Name the parasite shown.
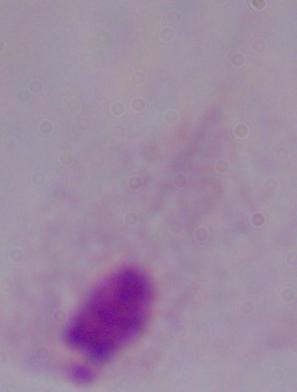
A trichomonad.

Micrograph. 1000x magnification.